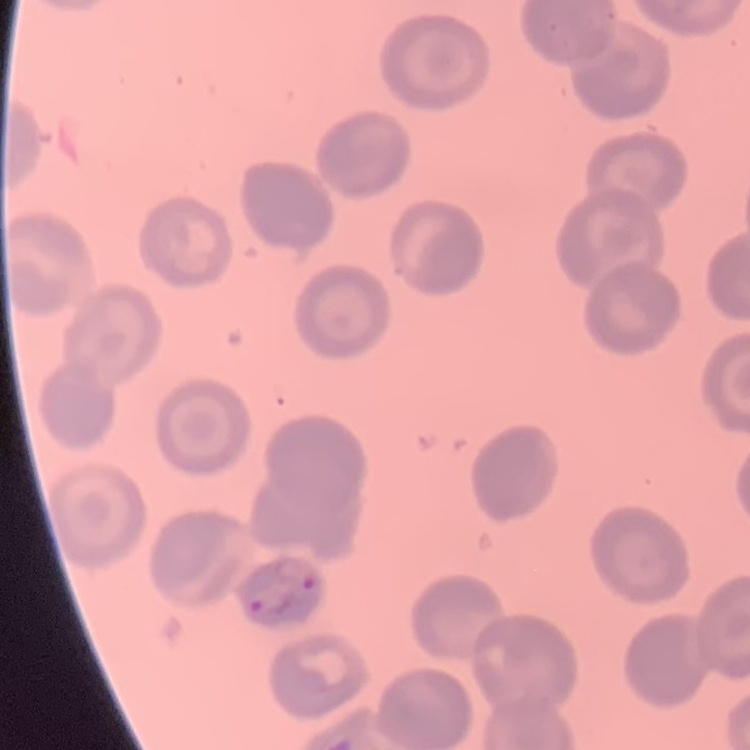

Summary:
  - Erythrocyte morphology: no rouleaux formation
  - Stain: Field's or Giemsa
  - Image type: one tile cut from a larger photomicrograph
  - Preparation: thin peripheral smear